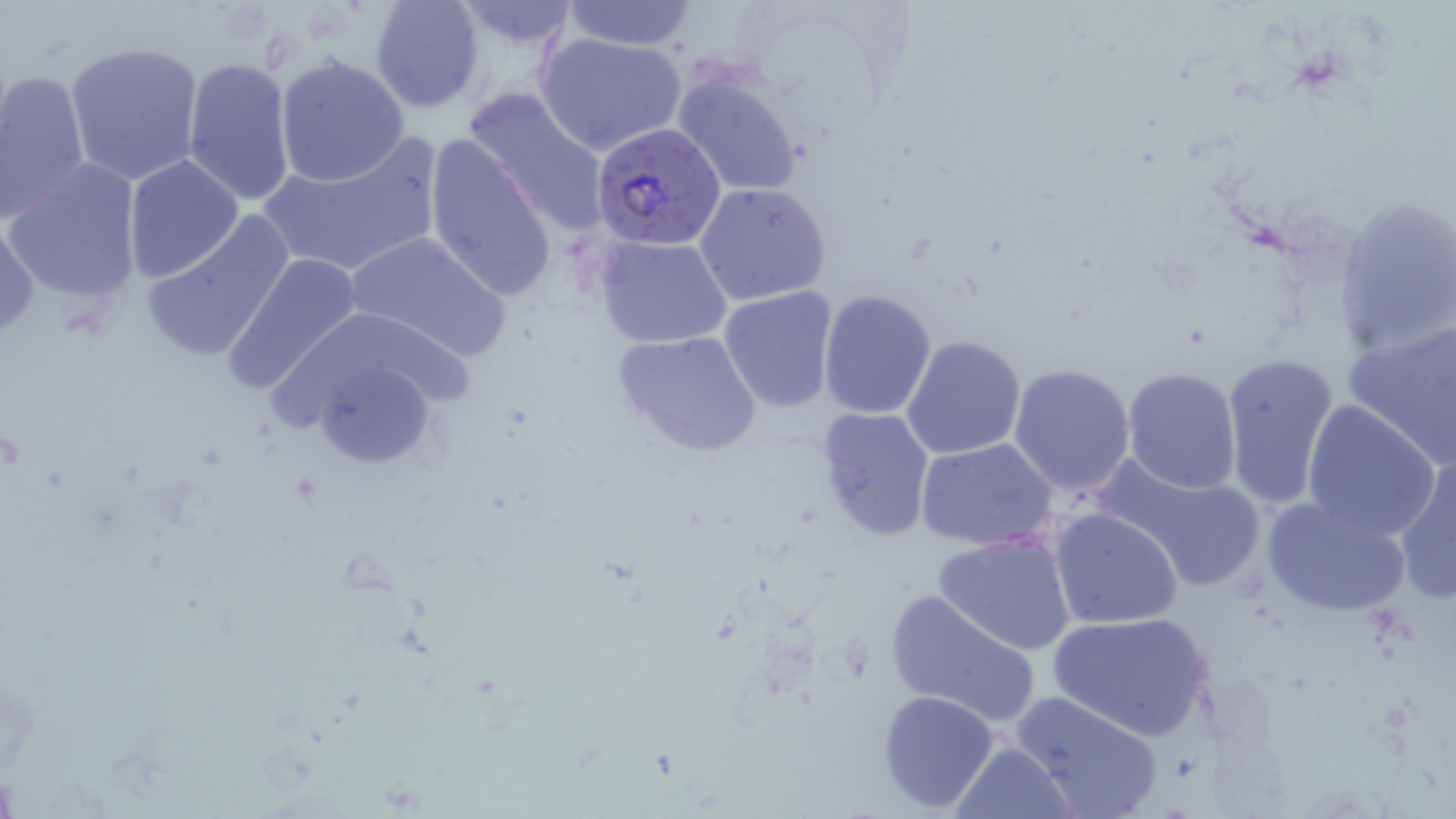
slide_level_diagnosis: Plasmodium falciparum
uninfected_red_blood_cell_locations: 'approximate bounding boxes as [x1, y1, x2, y2] in pixels: [370, 0, 485, 113], [560, 0, 696, 51], [451, 2, 580, 49], [537, 32, 687, 156], [65, 40, 204, 187], [275, 54, 410, 186], [181, 56, 296, 206], [0, 69, 90, 223], [673, 75, 803, 196], [466, 88, 610, 227], [257, 135, 446, 279], [423, 135, 558, 302], [123, 154, 245, 285], [5, 161, 145, 306], [695, 182, 832, 305], [1334, 197, 1455, 359], [140, 209, 296, 364], [0, 217, 42, 341], [343, 229, 512, 365], [594, 236, 732, 349], [222, 251, 364, 398], [717, 285, 839, 413], [817, 289, 939, 419], [267, 304, 469, 470], [1344, 317, 1456, 465], [612, 330, 763, 457], [901, 334, 1026, 461], [1219, 351, 1342, 512], [1007, 363, 1137, 498], [1121, 366, 1243, 494], [1300, 400, 1442, 540], [815, 406, 935, 544], [916, 438, 1060, 551], [1394, 450, 1456, 603], [1092, 454, 1271, 595], [1261, 493, 1410, 617], [1049, 508, 1183, 628], [934, 531, 1077, 654], [885, 588, 1042, 729], [1047, 611, 1213, 741], [877, 689, 1002, 811], [1009, 691, 1164, 819], [950, 741, 1078, 819]'
plasmodium_falciparum_infected_red_blood_cell_locations: 'approximate bounding boxes as [x1, y1, x2, y2] in pixels: [590, 118, 727, 251]'
field_of_view: single
stain: May-Grünwald-Giemsa
magnification: 1000x
image_size: 1456×819 pixels
preparation: thin blood smear
modality: optical microscopy